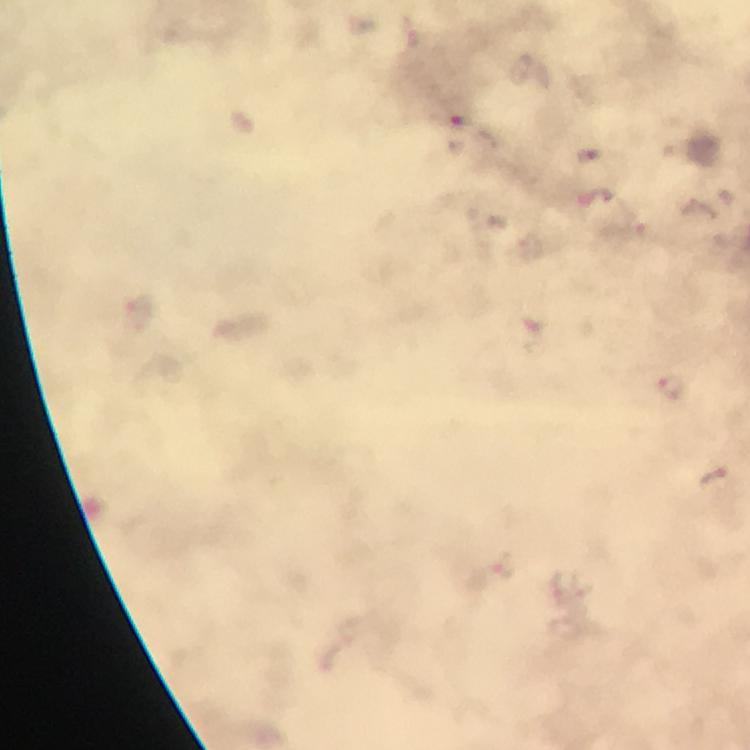
image_size: 750×750 pixels
preparation: thick smear
plasmodium_parasite_locations: 'approximate centers as [x, y] in pixels: [461, 119], [596, 197]'
capture: smartphone photograph through a microscope
context: from a malaria diagnostic workup
immersion_oil: applied
cropped_from: one field of view
stain: Giemsa
magnification: 100x